Point out each Plasmodium parasite.
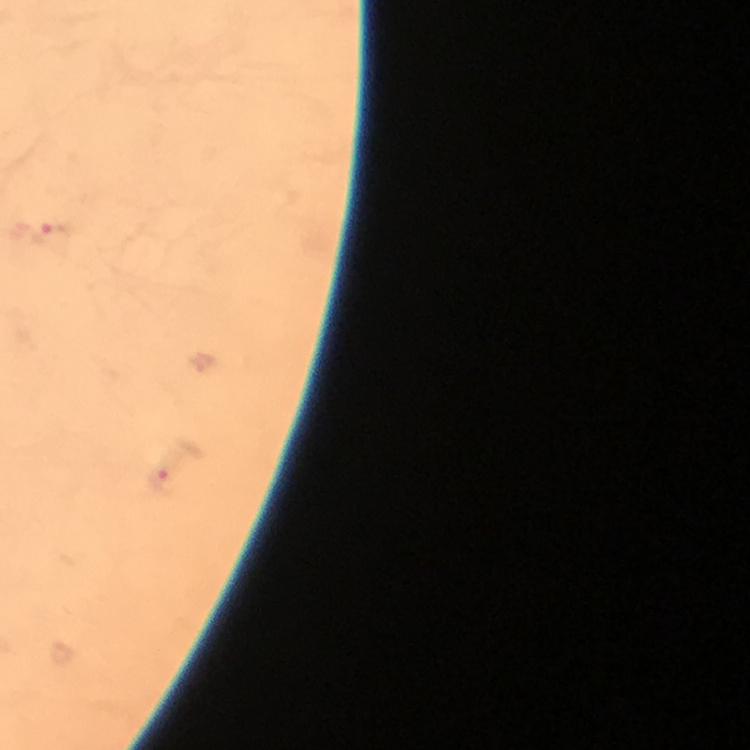
Approximate object centers, in pixels from the top-left corner.
Plasmodium parasites: (x=57, y=240), (x=166, y=481).

Summary:
  - Immersion oil: applied
  - Preparation: thick blood film
  - Capture: smartphone mounted on the microscope
  - Stain: Giemsa
  - Cropped from: a single field of view
  - Magnification: 100x
  - Context: from a diagnostic examination for malaria
  - Image size: 750×750 pixels